Assess this cell for malaria.
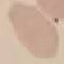
It is uninfected.

Summary:
  - Image type: automatically extracted cell patch, resized to 64 × 64 pixels
  - Capture: smartphone through the microscope eyepiece
  - Stain: Giemsa
  - Preparation: thin smear